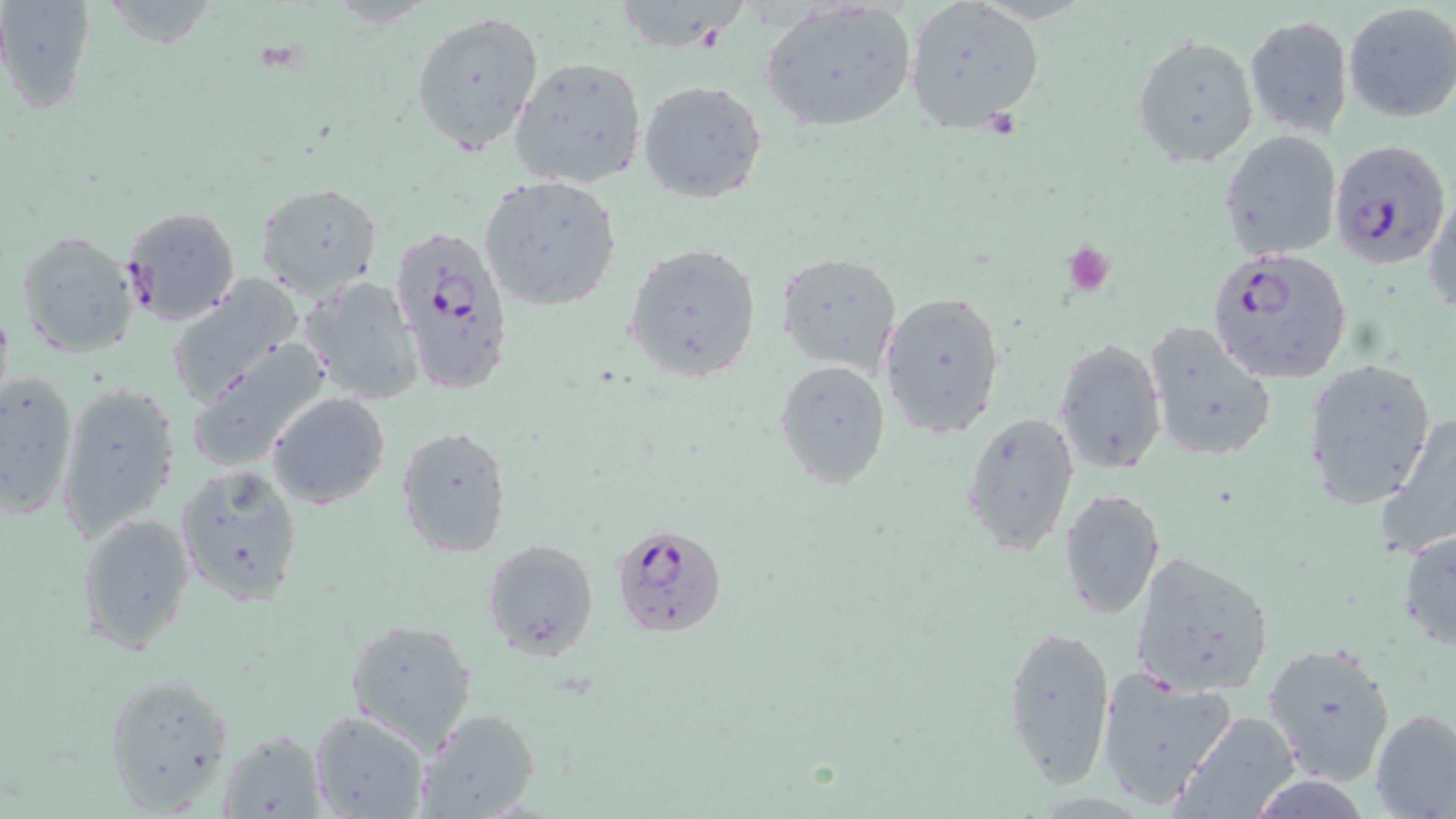

{
  "slide_level_diagnosis": "Plasmodium falciparum",
  "preparation": "thin blood smear",
  "modality": "optical microscopy",
  "magnification": "1000x",
  "stain": "May-Grünwald-Giemsa",
  "platelet_locations": "approximate bounding boxes as (x1, y1, x2, y2) in pixels: (1061, 242, 1116, 295)",
  "field_of_view": "single",
  "uninfected_red_blood_cell_locations": "approximate bounding boxes as (x1, y1, x2, y2) in pixels: (0, 1, 94, 115), (905, 1, 1044, 132), (625, 2, 748, 56), (760, 3, 917, 132), (1344, 3, 1456, 122), (411, 10, 545, 154), (1245, 15, 1353, 137), (1131, 34, 1258, 168), (509, 56, 647, 189), (638, 80, 769, 203), (1219, 131, 1343, 259), (479, 174, 624, 310), (253, 180, 383, 301), (1425, 190, 1455, 318), (15, 234, 142, 361), (626, 240, 765, 382), (778, 252, 904, 373), (166, 275, 307, 404), (297, 276, 424, 405), (878, 289, 1006, 439), (1144, 322, 1277, 463), (1055, 339, 1166, 473), (185, 340, 332, 473), (1306, 358, 1436, 510), (773, 361, 891, 491), (0, 369, 78, 521), (56, 379, 182, 542), (268, 392, 391, 509), (961, 411, 1079, 556), (1377, 416, 1456, 563), (396, 425, 512, 557), (176, 462, 303, 604), (1059, 488, 1166, 619), (76, 510, 195, 652), (1396, 527, 1456, 657), (482, 538, 599, 659), (1131, 555, 1275, 696), (347, 619, 477, 742), (1001, 623, 1116, 794), (1261, 640, 1398, 786), (1094, 665, 1240, 806), (101, 673, 235, 814), (1371, 707, 1456, 817), (417, 708, 539, 816), (311, 710, 429, 818), (1171, 710, 1301, 819), (220, 731, 324, 817)",
  "image_size": "1456×819 pixels",
  "plasmodium_falciparum_infected_red_blood_cell_locations": "approximate bounding boxes as (x1, y1, x2, y2) in pixels: (1329, 138, 1451, 268), (118, 206, 243, 327), (388, 222, 512, 392), (1211, 246, 1352, 384), (612, 521, 728, 638)"
}